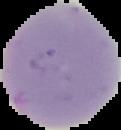
{
  "preparation": "thin blood film",
  "malaria_status": "uninfected",
  "image_size": "121×130 pixels",
  "image_type": "cell region segmented out of the field of view; surrounding area masked to black"
}